Locate every Plasmodium falciparum-infected red blood cell.
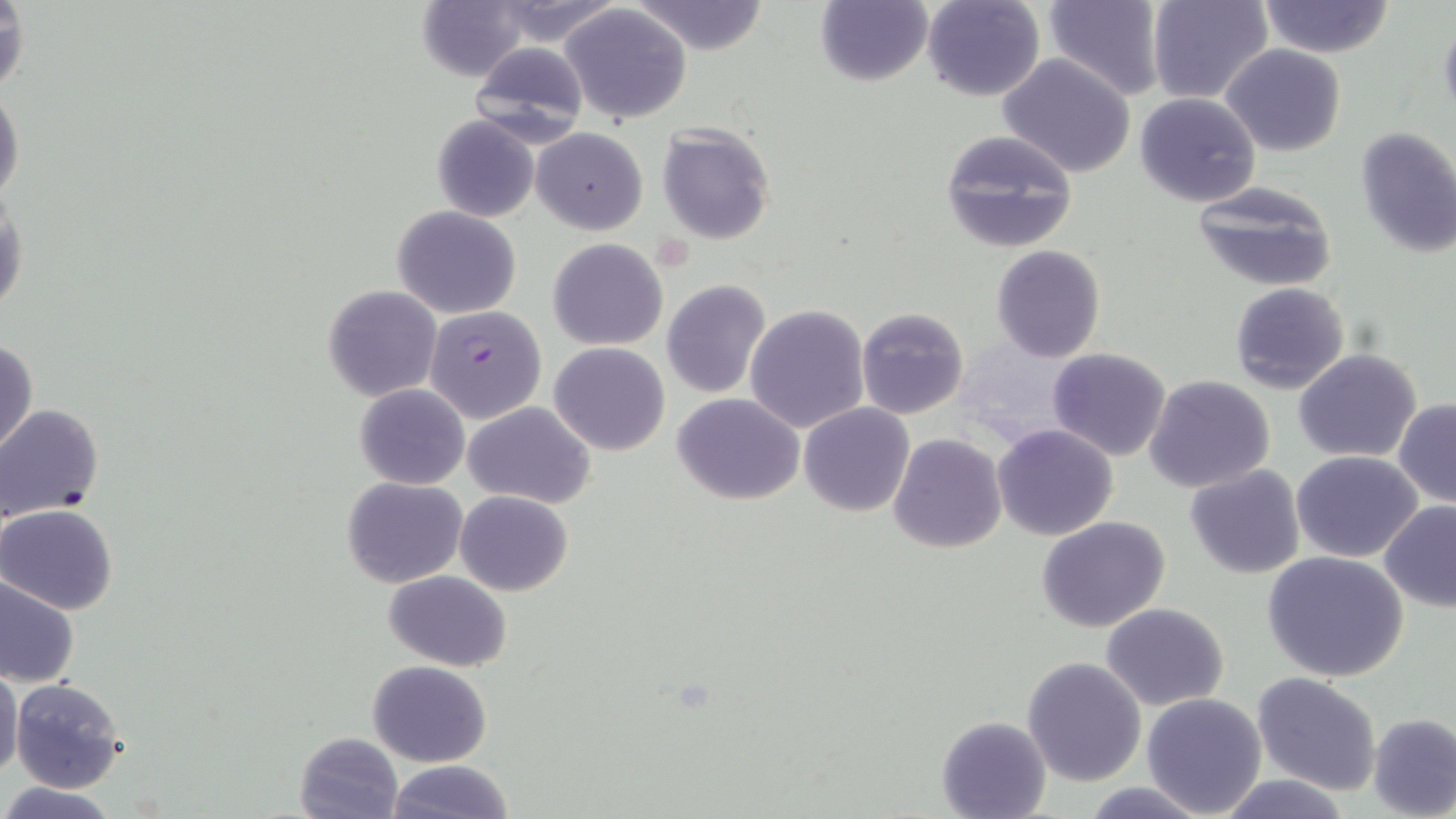
Approximate bounding boxes as (x1,y1)-(x2,y2) corner pairs in pixels.
Plasmodium falciparum-infected red blood cells: (423,305)-(547,423).

Summary:
  - Uninfected red blood cell locations: (487,0)-(626,49), (631,0)-(772,55), (921,0)-(1045,102), (1149,0)-(1273,104), (412,1)-(536,82), (814,1)-(932,86), (1041,1)-(1165,98), (1258,1)-(1394,57), (0,2)-(29,100), (560,3)-(693,123), (1437,14)-(1456,123), (468,41)-(590,143), (1221,45)-(1346,156), (998,52)-(1137,178), (0,83)-(24,205), (1135,92)-(1260,208), (432,115)-(539,222), (657,124)-(776,244), (1353,125)-(1456,258), (533,126)-(648,234), (939,130)-(1078,253), (1191,180)-(1339,292), (0,193)-(28,319), (391,205)-(522,319), (548,239)-(667,351), (991,245)-(1107,364), (661,280)-(770,398), (1230,282)-(1350,393), (322,285)-(441,401), (1246,302)-(1383,438), (745,304)-(870,433), (857,307)-(970,420), (1,339)-(37,459), (549,342)-(670,455), (1047,348)-(1173,461), (1293,349)-(1422,461), (1145,375)-(1276,493), (354,383)-(469,489), (673,393)-(805,506), (1394,398)-(1456,508), (464,401)-(595,509), (0,403)-(105,524), (798,403)-(915,517), (992,424)-(1119,540), (888,434)-(1006,554), (1292,450)-(1424,563), (1184,465)-(1307,580), (342,477)-(467,588), (455,490)-(574,596), (1379,501)-(1456,613), (2,505)-(118,614), (1037,517)-(1170,633), (1262,552)-(1410,683), (383,570)-(513,670), (0,573)-(79,687), (1101,603)-(1230,711), (1022,657)-(1148,787), (367,661)-(494,766), (0,665)-(23,780), (1252,671)-(1382,794), (9,678)-(127,792), (1141,693)-(1268,817), (1368,712)-(1456,818), (937,715)-(1050,818), (295,731)-(403,817), (386,759)-(514,818), (1215,774)-(1355,818), (1,782)-(117,819), (1080,782)-(1214,817)
  - Slide-level diagnosis: Plasmodium falciparum
  - Preparation: thin blood film
  - Stain: May-Grünwald-Giemsa
  - Modality: optical microscopy
  - Field of view: single
  - Image size: 1456×819 pixels
  - Magnification: 1000x